Assess the morphology of the erythrocytes.
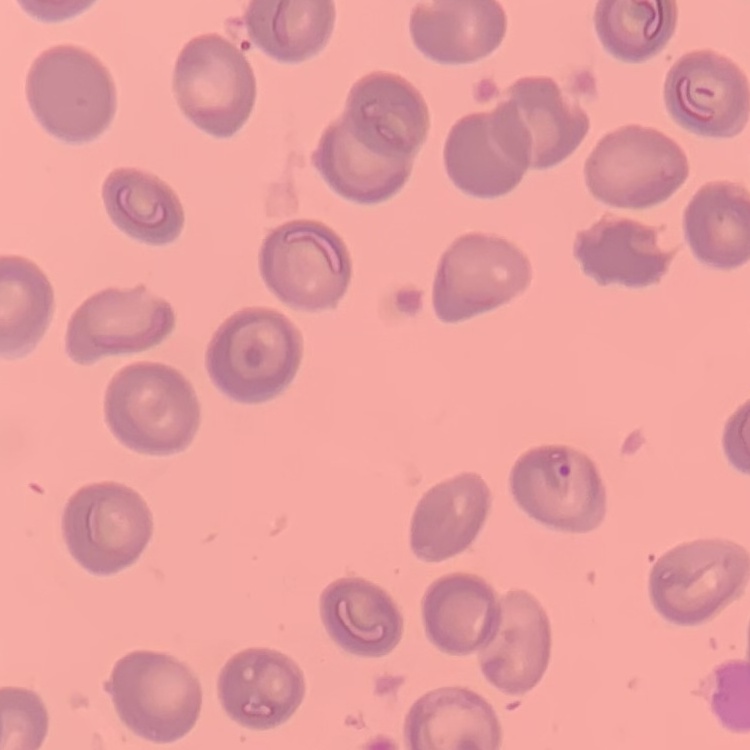

They show no rouleaux formation.

stain = Field's or Giemsa
preparation = thin blood smear
image type = square crop of a larger photomicrograph